Assess the morphology of the red blood cells.
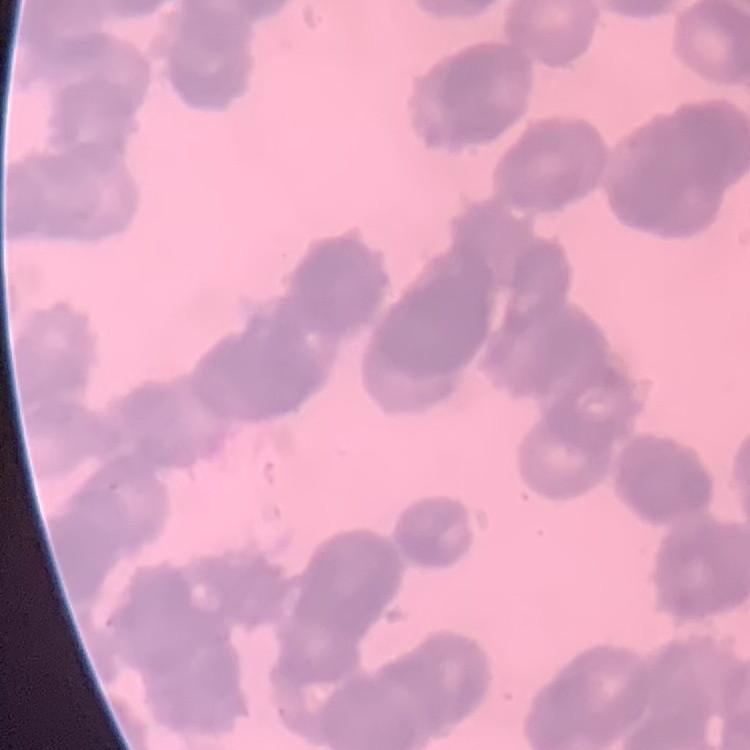

They show rouleaux formation.

stain = Field's or Giemsa
image type = square crop of a larger photomicrograph
preparation = thin blood smear